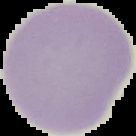

From a thin blood film. Image is 136×136 pixels. The area outside the segmented cell region is set to black. Result: negative for Plasmodium parasites.